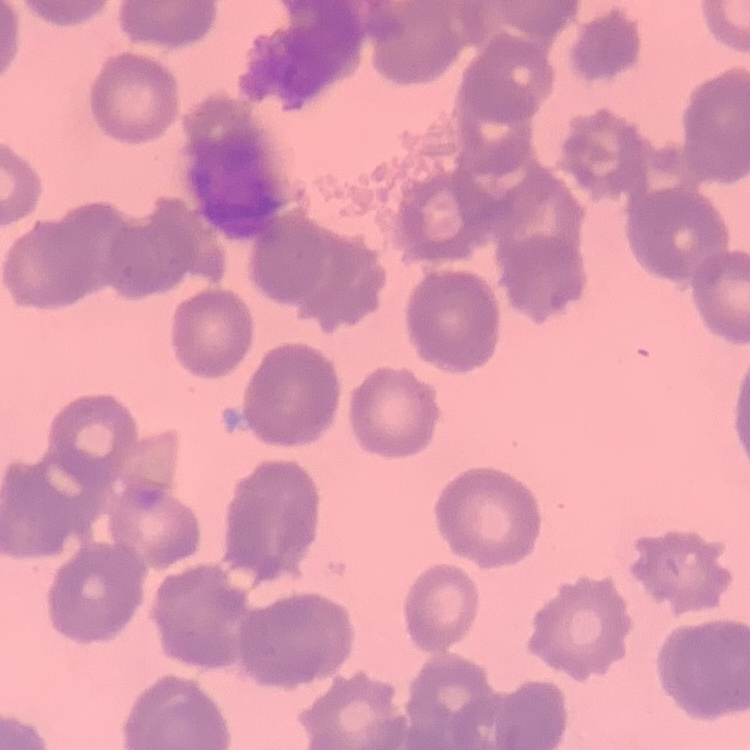 The red blood cells exhibit rouleaux formation. Stained with either Field's or Giemsa. One tile cut from a larger photomicrograph. Thin blood film.